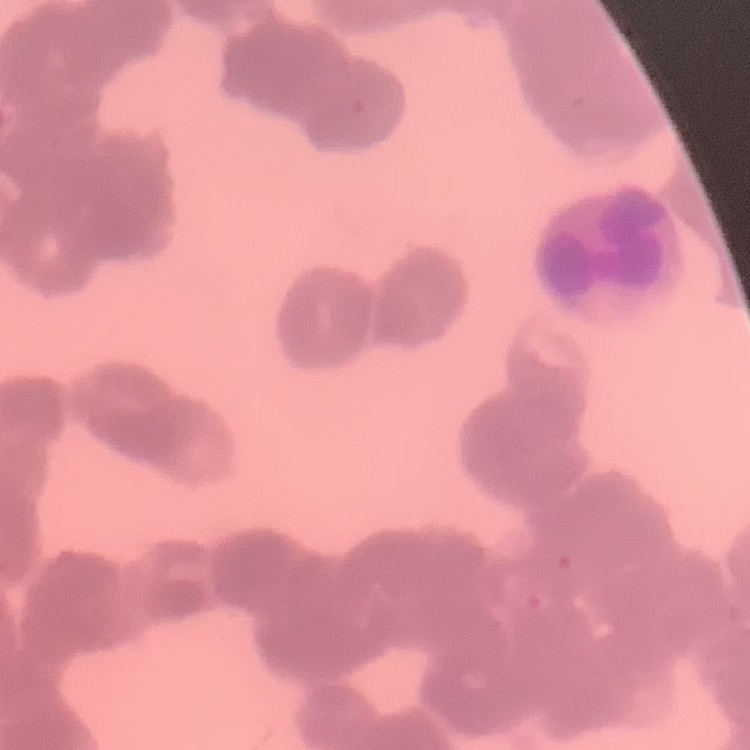
Summary:
  - Red blood cell morphology: rouleaux formation
  - Preparation: thin blood film
  - Stain: Field's or Giemsa
  - Image type: one tile cut from a larger photomicrograph